Assess the morphology of the erythrocytes.
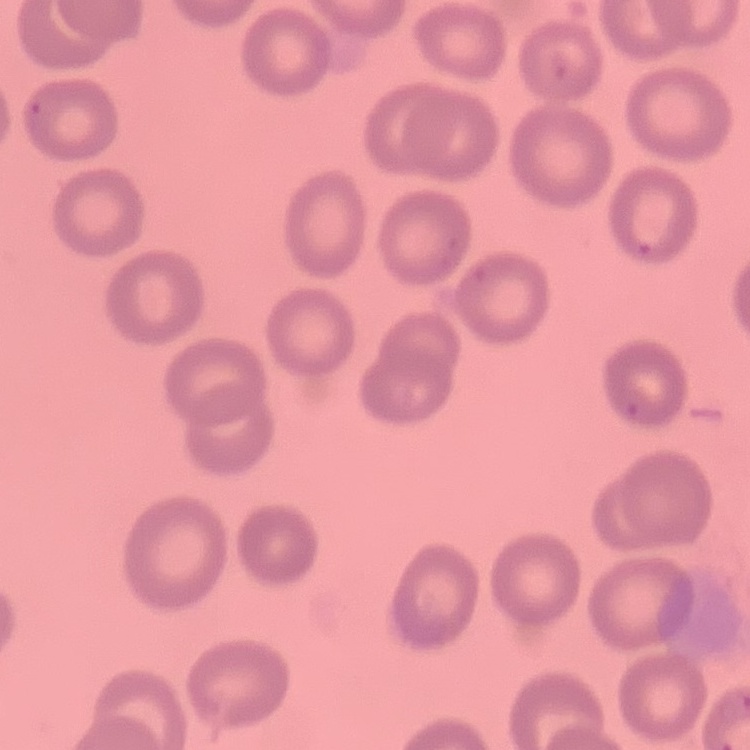

No rouleaux formation.

Summary:
  - Stain: Field's or Giemsa
  - Image type: square crop of a larger photomicrograph
  - Preparation: thin peripheral smear